State which parasite is depicted.
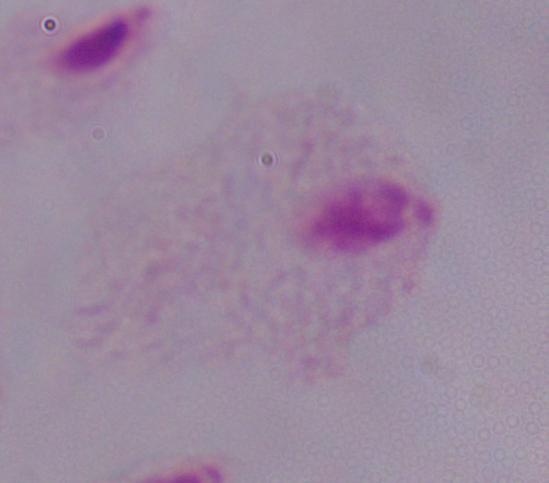
This is a trichomonad.

Summary:
  - Magnification: 1000x
  - Modality: photomicrograph